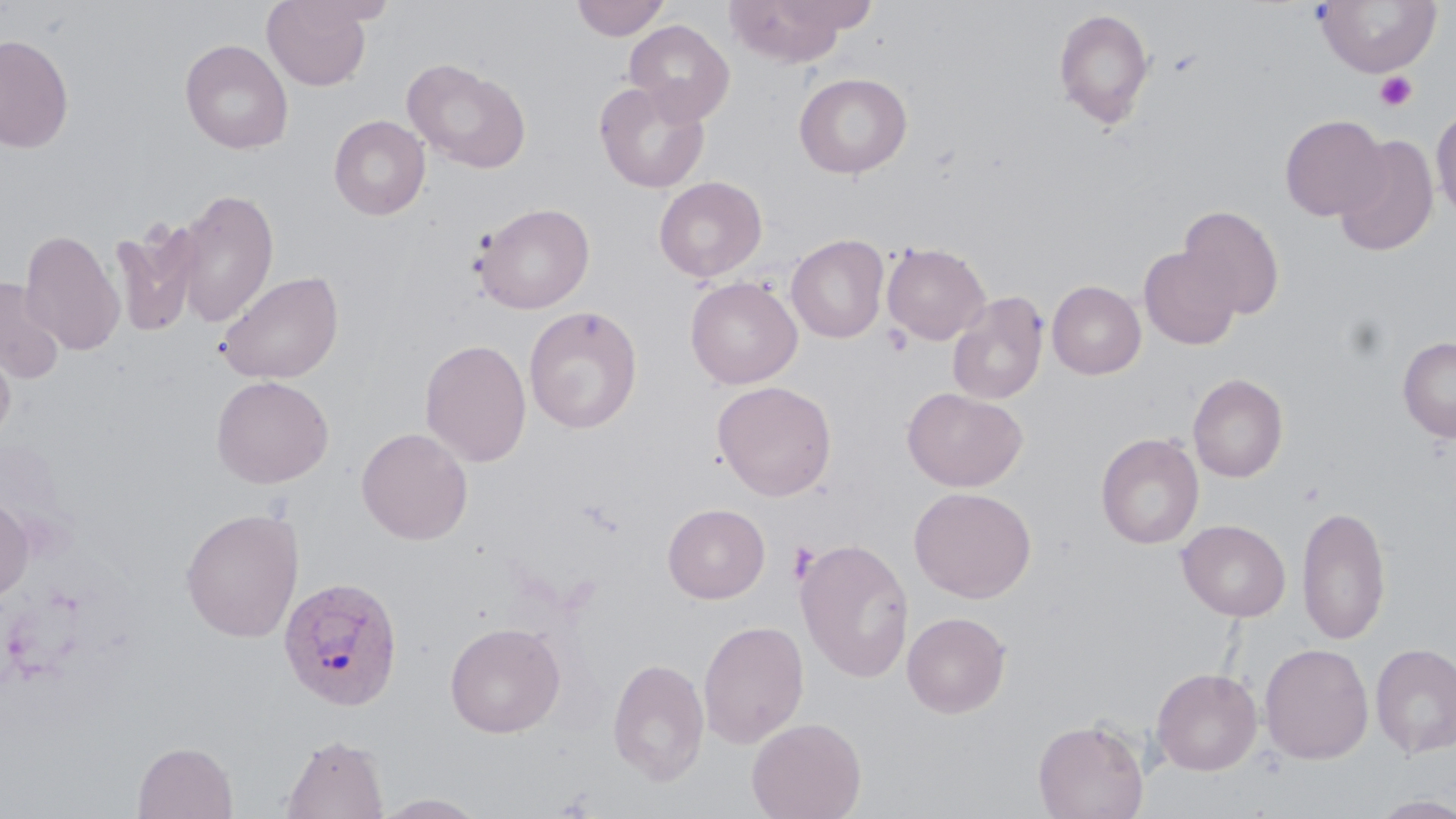
slide-level diagnosis = Plasmodium ovale
uninfected red blood cell locations = approximate bounding boxes as [x1, y1, x2, y2] in pixels: [262, 0, 373, 90], [571, 0, 671, 41], [723, 0, 867, 67], [1313, 1, 1442, 77], [1053, 8, 1155, 130], [624, 20, 735, 124], [0, 35, 73, 153], [180, 39, 293, 154], [402, 58, 532, 174], [794, 72, 913, 178], [594, 80, 710, 193], [1431, 106, 1456, 218], [1280, 114, 1388, 221], [329, 115, 430, 220], [1334, 134, 1439, 256], [654, 176, 767, 283], [173, 188, 280, 327], [475, 203, 595, 314], [1178, 205, 1285, 320], [109, 221, 202, 338], [19, 228, 126, 356], [786, 234, 889, 343], [882, 242, 991, 345], [1139, 246, 1242, 350], [216, 269, 344, 384], [685, 276, 802, 389], [1, 278, 64, 384], [1047, 280, 1146, 379], [947, 291, 1048, 405], [524, 305, 643, 434], [1398, 336, 1456, 442], [0, 338, 15, 449], [420, 338, 532, 467], [1188, 373, 1288, 482], [210, 375, 334, 488], [713, 380, 837, 501], [902, 387, 1027, 492], [356, 427, 473, 544], [1096, 433, 1204, 549], [909, 486, 1036, 603], [0, 498, 35, 602], [662, 503, 770, 603], [1296, 504, 1392, 645], [180, 508, 304, 642], [1177, 519, 1291, 621], [796, 538, 914, 682], [902, 611, 1011, 718], [697, 619, 810, 748], [444, 622, 565, 738], [1259, 643, 1374, 763], [1370, 643, 1456, 758], [608, 658, 710, 785], [1151, 667, 1263, 776], [747, 717, 866, 819], [1033, 718, 1150, 819], [281, 733, 388, 819], [133, 741, 238, 819], [373, 793, 489, 818], [1369, 795, 1456, 818]
modality = light microscopy
magnification = 1000x
preparation = thin blood smear
platelet locations = approximate bounding boxes as [x1, y1, x2, y2] in pixels: [1374, 71, 1418, 112], [788, 540, 820, 584]
image size = 1456×819 pixels
stain = May-Grünwald-Giemsa
Plasmodium ovale-infected red blood cell locations = approximate bounding boxes as [x1, y1, x2, y2] in pixels: [278, 575, 404, 711]
field of view = single